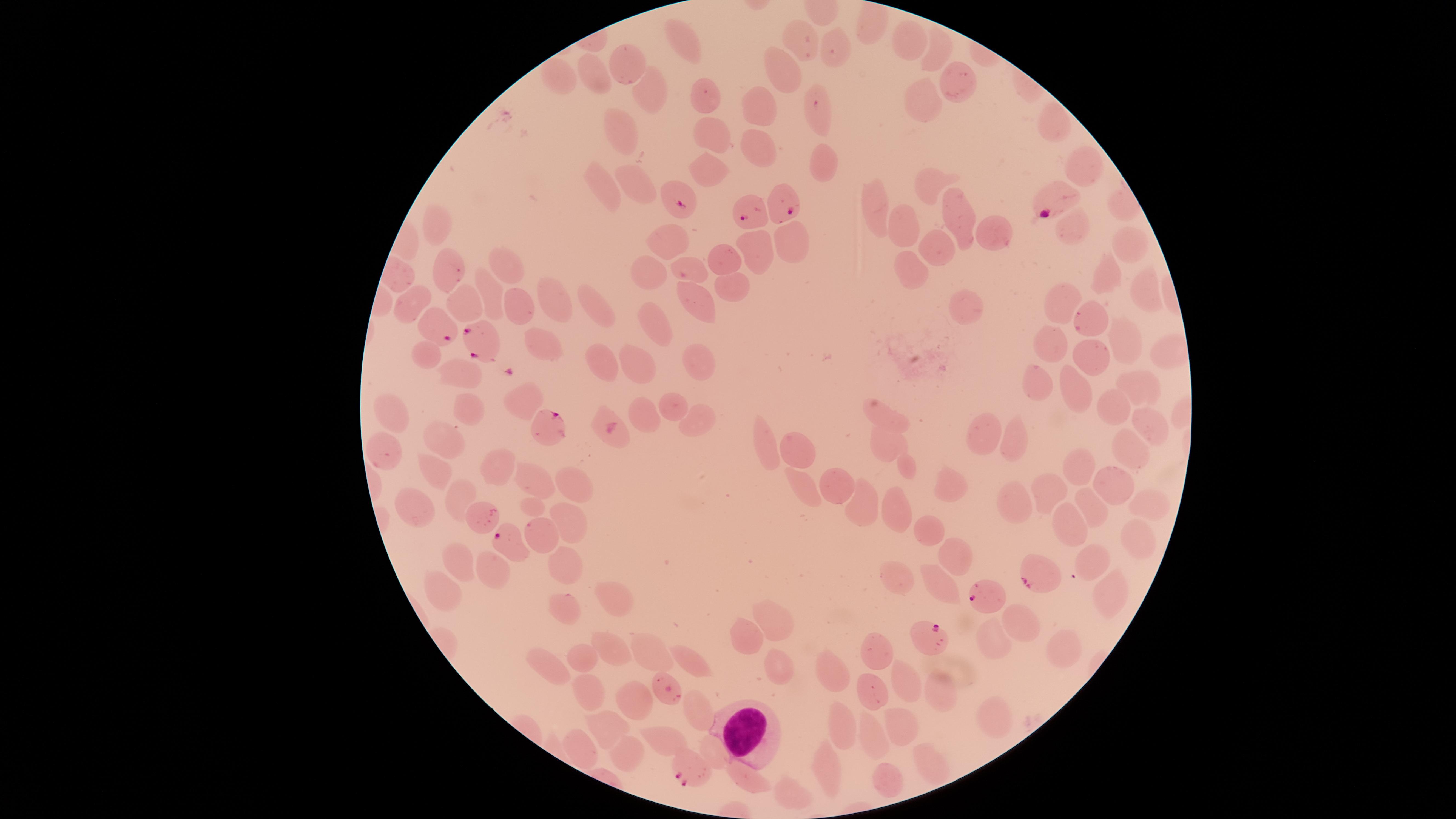

{
  "image_size": "1456×819 pixels",
  "uninfected_red_blood_cells": "approximate marker points as [x, y] in pixels: [869, 29], [685, 37], [799, 39], [910, 42], [842, 45], [942, 47], [626, 57], [599, 69], [563, 72], [787, 74], [960, 81], [647, 93], [707, 94], [925, 101], [766, 103], [822, 103], [1051, 124], [626, 134], [715, 137], [762, 152], [822, 164], [1084, 166], [707, 176], [606, 183], [928, 185], [637, 187], [875, 205], [959, 212], [909, 226], [1071, 229], [438, 230], [996, 236], [788, 240], [1127, 240], [670, 241], [756, 248], [938, 249], [725, 257], [693, 266], [656, 268], [508, 270], [445, 272], [912, 272], [1109, 272], [731, 286], [1146, 289], [493, 297], [550, 297], [696, 301], [408, 302], [600, 302], [1062, 303], [463, 306], [516, 308], [965, 310], [660, 318], [1093, 319], [1123, 338], [1050, 347], [541, 351], [605, 352], [427, 354], [701, 358], [1089, 358], [643, 362], [463, 372], [1038, 379], [1133, 380], [1077, 381], [523, 397], [672, 402], [467, 405], [1111, 406], [644, 416], [697, 416], [893, 416], [394, 417], [1146, 418], [979, 431], [887, 439], [1013, 439], [448, 441], [764, 445], [389, 447], [798, 447], [1130, 447], [505, 463], [1085, 463], [433, 469], [908, 469], [536, 481], [1109, 483], [834, 484], [954, 484], [807, 486], [577, 487], [1050, 487], [464, 497], [1018, 499], [860, 501], [531, 504], [416, 505], [897, 505], [1092, 505], [1145, 510], [475, 514], [1069, 523], [570, 524], [930, 532], [538, 535], [1133, 539], [956, 552], [1085, 559], [458, 560], [565, 560], [500, 565], [896, 576], [934, 583], [613, 594], [1106, 594], [440, 596], [565, 607], [775, 617], [1018, 619], [752, 629], [992, 643], [1059, 647], [648, 649], [614, 650], [879, 651], [583, 655], [553, 659], [693, 662], [780, 667], [830, 667], [912, 679], [936, 686], [871, 687], [584, 689], [633, 695], [698, 714], [990, 717], [840, 721], [901, 721], [608, 723], [873, 737], [667, 738], [711, 744], [577, 748], [625, 749], [929, 764], [821, 769], [888, 780], [743, 784], [782, 793]",
  "visible_region": "circular",
  "white_blood_cells": "approximate marker points as [x, y] in pixels: [742, 724]",
  "capture": "smartphone photograph through the microscope eyepiece",
  "species": "Plasmodium falciparum",
  "field_of_view": "single",
  "presence": "malaria parasites detected",
  "parasitized_red_blood_cells": "approximate marker points as [x, y] in pixels: [678, 199], [1052, 199], [783, 201], [750, 212], [437, 328], [477, 342], [545, 427], [508, 538], [1034, 575], [983, 600], [928, 641], [669, 689], [686, 770]",
  "stain": "Giemsa",
  "preparation": "thin smear of blood"
}